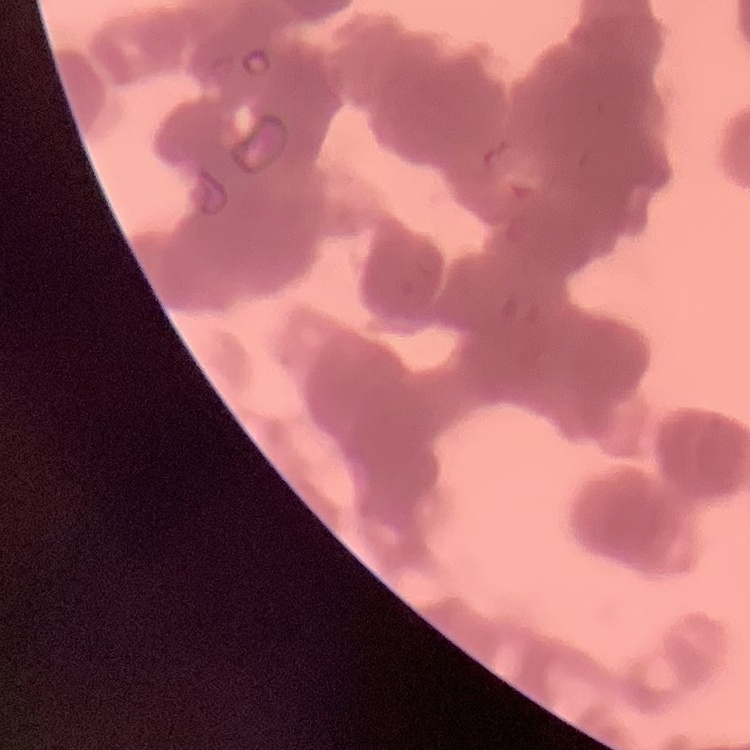
Summary:
  - Red blood cell morphology: rouleaux formation
  - Image type: square crop of a larger photomicrograph
  - Preparation: thin peripheral smear
  - Stain: Field's or Giemsa